Outline platelets.
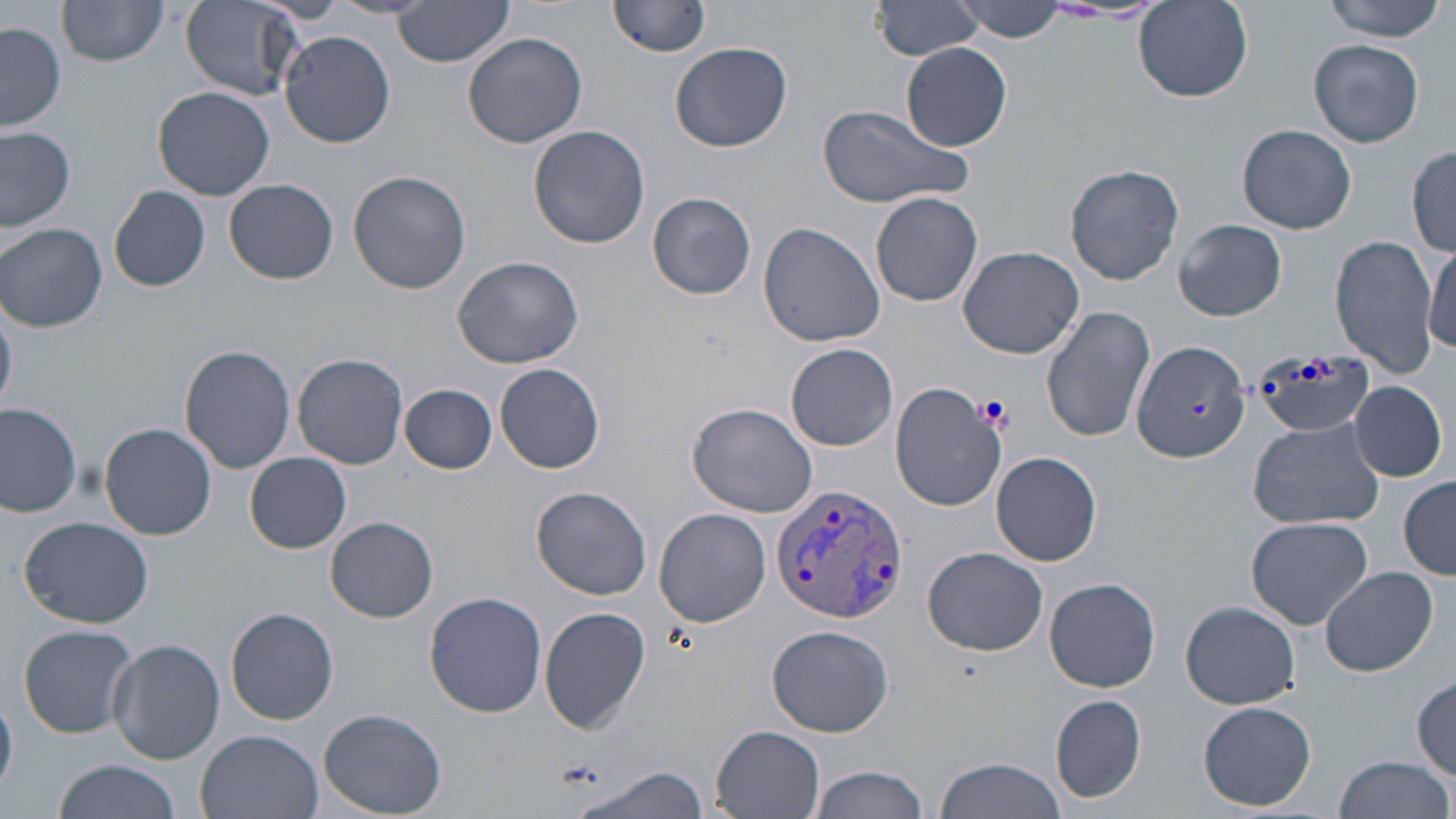

Approximate bounding boxes as (x1,y1)-(x2,y2) corner pairs in pixels.
Platelets: (1188,400)-(1210,418).

Plasmodium vivax-infected red blood cell locations: (769,485)-(910,624). Uninfected red blood cell locations: (180,0)-(306,100), (392,0)-(516,66), (611,0)-(714,56), (874,0)-(986,59), (1319,0)-(1449,41), (952,1)-(1069,41), (57,2)-(169,67), (1134,2)-(1253,102), (1,19)-(68,132), (279,30)-(397,147), (462,30)-(586,149), (1309,37)-(1425,148), (670,41)-(793,152), (902,44)-(1015,150), (152,87)-(274,201), (816,103)-(972,209), (1237,123)-(1357,234), (0,125)-(77,232), (529,125)-(651,247), (1408,145)-(1455,257), (1064,163)-(1185,285), (348,171)-(471,294), (226,179)-(338,284), (109,185)-(209,292), (648,192)-(758,299), (871,192)-(983,306), (1175,219)-(1287,322), (1,221)-(107,333), (758,221)-(885,348), (1332,234)-(1440,377), (1426,239)-(1456,353), (959,247)-(1087,359), (453,256)-(583,367), (1041,305)-(1156,444), (1130,338)-(1250,464), (786,344)-(898,451), (180,345)-(296,473), (293,354)-(408,468), (494,363)-(605,473), (1350,380)-(1446,481), (400,383)-(497,474), (889,385)-(1004,509), (0,399)-(81,519), (688,401)-(819,517), (1247,416)-(1386,531), (99,424)-(216,539), (992,451)-(1101,566), (244,452)-(351,554), (1400,477)-(1456,578), (530,485)-(653,599), (654,508)-(771,627), (327,514)-(438,621), (19,515)-(153,629), (1244,516)-(1374,629), (922,545)-(1049,656), (1320,567)-(1437,678), (1044,577)-(1162,692), (424,591)-(548,719), (1181,601)-(1300,709), (226,606)-(339,725), (539,607)-(651,733), (766,623)-(894,735), (17,624)-(139,739), (108,638)-(224,763), (1412,674)-(1456,778), (1,693)-(18,801), (1050,695)-(1146,804), (1199,701)-(1316,811), (317,707)-(448,816), (711,727)-(825,818), (197,729)-(326,819), (1334,754)-(1454,819), (934,757)-(1070,819), (53,758)-(187,819), (569,763)-(710,819), (810,764)-(930,819). Slide-level diagnosis: Plasmodium vivax. Thin blood film. 1000x magnification. May-Grünwald-Giemsa-stained preparation. Image is 1456×819 pixels. Light microscopy. One field of a larger specimen.